Give the preparation type.
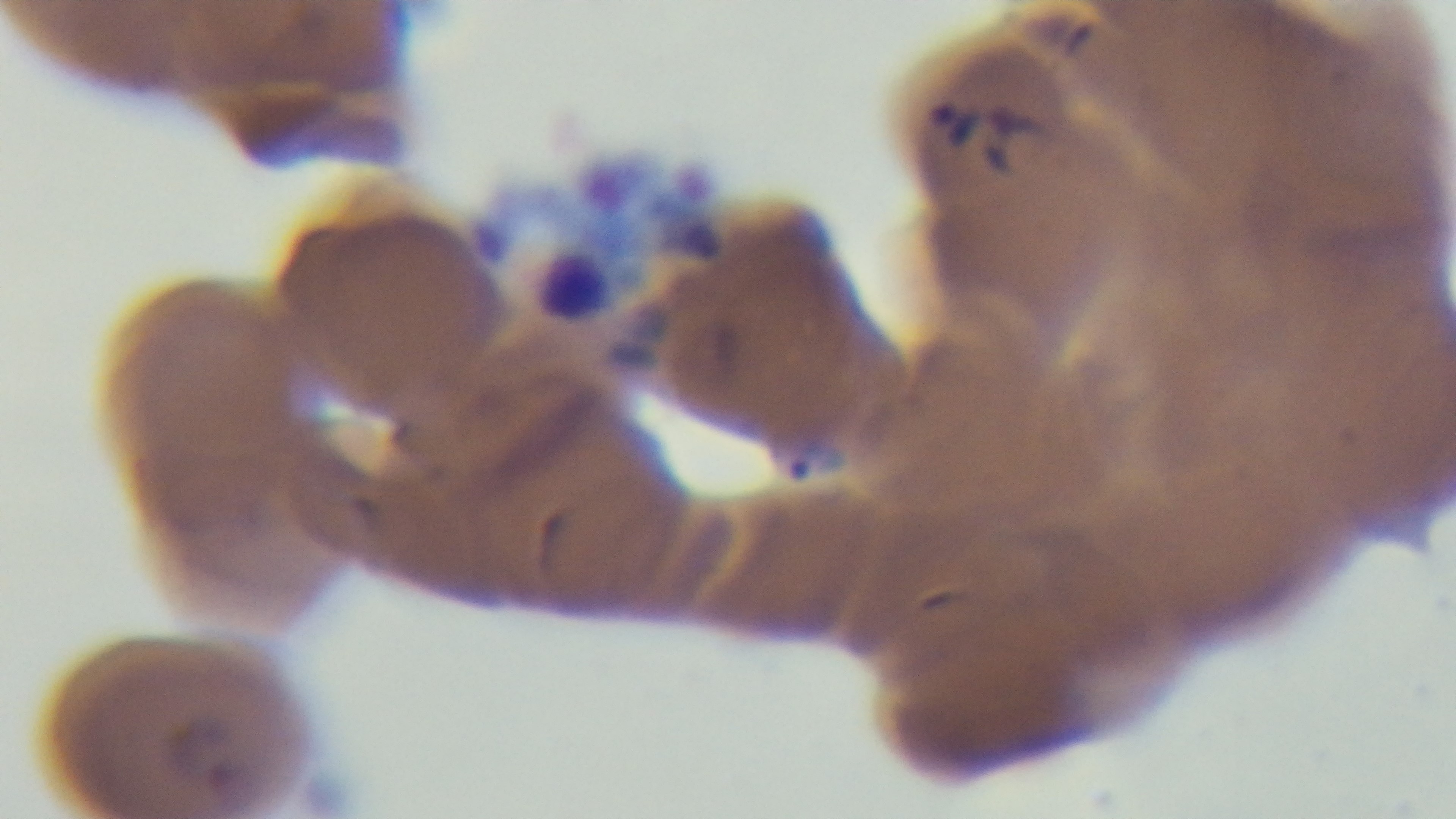
A thin smear.

Summary:
  - Capture: mounted 4K digital camera
  - Stain: Giemsa
  - Field of view: single
  - Modality: light microscopy
  - Malaria status: infected
  - Objective: 100x oil immersion